Find each parasitized red blood cell.
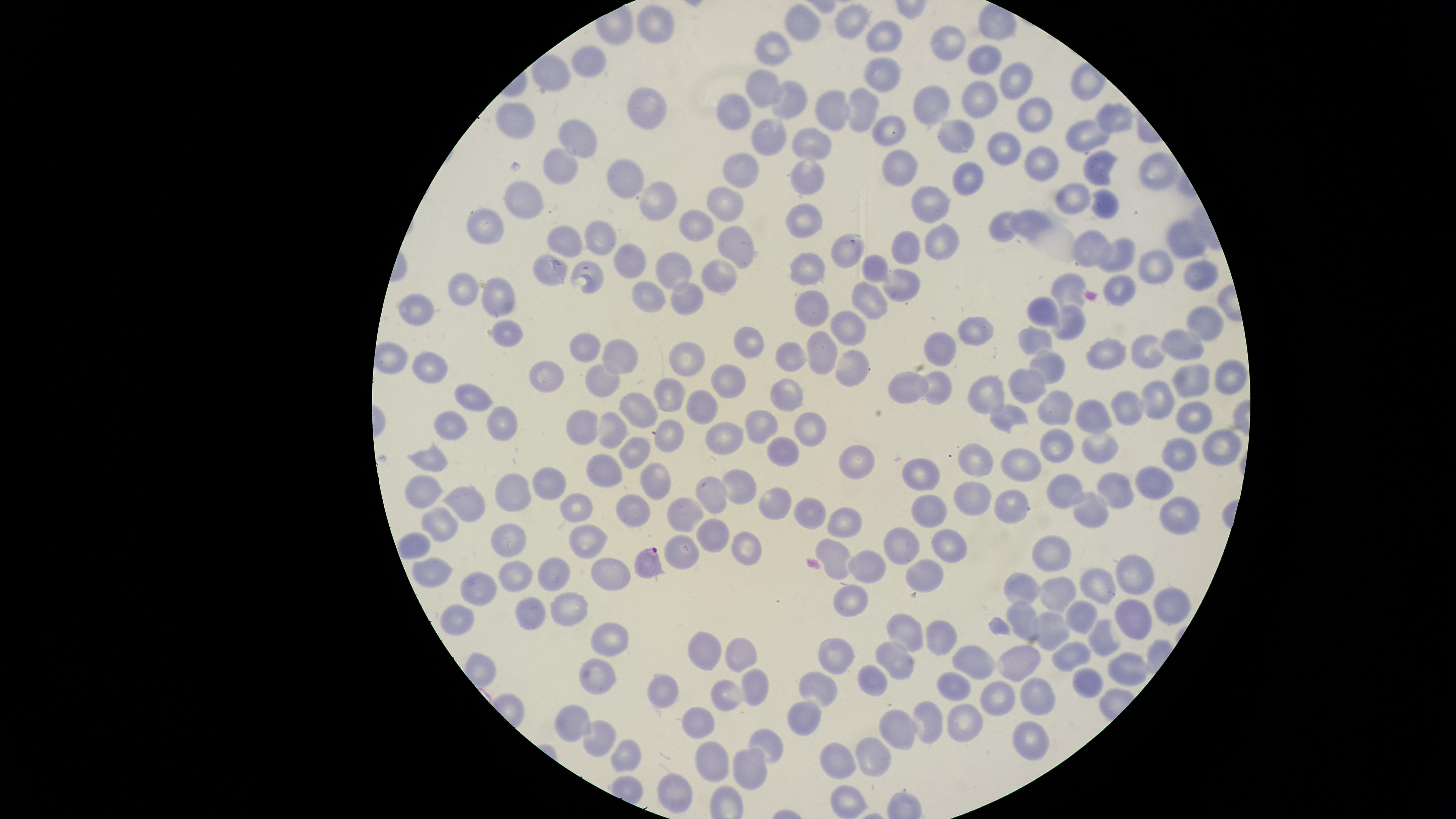
Approximate marker points, in pixels from the top-left corner.
Parasitized red blood cells: (x=644, y=564).

Approximate marker points, in pixels from the top-left corner. Uninfected red blood cells: (x=806, y=20), (x=853, y=20), (x=656, y=29), (x=889, y=32), (x=951, y=41), (x=779, y=48), (x=981, y=63), (x=592, y=64), (x=885, y=76), (x=1009, y=77), (x=765, y=81), (x=974, y=95), (x=796, y=101), (x=939, y=101), (x=742, y=109), (x=1034, y=109), (x=647, y=111), (x=838, y=112), (x=863, y=112), (x=1109, y=120), (x=517, y=121), (x=770, y=131), (x=957, y=134), (x=577, y=135), (x=892, y=135), (x=805, y=137), (x=1087, y=137), (x=1001, y=149), (x=571, y=158), (x=1040, y=164), (x=1150, y=168), (x=744, y=169), (x=1099, y=169), (x=898, y=172), (x=972, y=175), (x=805, y=179), (x=629, y=186), (x=1074, y=194), (x=928, y=200), (x=655, y=201), (x=1109, y=201), (x=522, y=202), (x=727, y=202), (x=1025, y=221), (x=805, y=223), (x=490, y=225), (x=693, y=225), (x=1003, y=232), (x=605, y=238), (x=942, y=238), (x=905, y=241), (x=560, y=242), (x=1181, y=242), (x=738, y=246), (x=1088, y=248), (x=847, y=250), (x=1121, y=252), (x=873, y=263), (x=632, y=264), (x=674, y=265), (x=1153, y=265), (x=551, y=268), (x=720, y=268), (x=809, y=268), (x=588, y=269), (x=1198, y=273), (x=903, y=278), (x=1123, y=286), (x=1065, y=287), (x=464, y=293), (x=651, y=293), (x=872, y=294), (x=689, y=295), (x=498, y=298), (x=813, y=302), (x=1045, y=305), (x=417, y=313), (x=1068, y=318), (x=852, y=320), (x=1204, y=327), (x=506, y=328), (x=974, y=335), (x=1038, y=337), (x=1184, y=342), (x=759, y=344), (x=942, y=346), (x=822, y=347), (x=583, y=348), (x=1144, y=352), (x=794, y=355), (x=619, y=356), (x=1109, y=361), (x=1050, y=362), (x=687, y=363), (x=848, y=363), (x=432, y=369), (x=1232, y=376), (x=549, y=377), (x=726, y=377), (x=602, y=379), (x=1191, y=381), (x=907, y=385), (x=1026, y=386), (x=940, y=388), (x=792, y=393), (x=661, y=394), (x=470, y=395), (x=986, y=395), (x=1155, y=395), (x=1061, y=404), (x=639, y=405), (x=703, y=405), (x=1122, y=408), (x=1097, y=414), (x=1198, y=415), (x=1006, y=416), (x=763, y=419), (x=499, y=425), (x=615, y=425), (x=448, y=427), (x=579, y=428), (x=813, y=431), (x=668, y=433), (x=725, y=434), (x=1060, y=441), (x=785, y=447), (x=631, y=448), (x=1102, y=449), (x=1229, y=449), (x=1174, y=454), (x=969, y=456), (x=858, y=458), (x=429, y=463), (x=1015, y=464), (x=605, y=467), (x=651, y=478), (x=924, y=479), (x=1153, y=480), (x=551, y=485), (x=735, y=485), (x=713, y=489), (x=1120, y=489), (x=1069, y=491), (x=518, y=493), (x=423, y=495), (x=971, y=497), (x=1005, y=502), (x=576, y=503), (x=632, y=506), (x=777, y=506), (x=463, y=508), (x=683, y=509), (x=812, y=511), (x=1174, y=512), (x=929, y=514), (x=1091, y=514), (x=843, y=518), (x=441, y=530), (x=712, y=535), (x=512, y=539), (x=418, y=543), (x=588, y=543), (x=899, y=543), (x=946, y=544), (x=684, y=547), (x=1059, y=547), (x=743, y=549), (x=836, y=552), (x=867, y=563), (x=550, y=568), (x=611, y=569), (x=435, y=572), (x=1132, y=572), (x=519, y=573), (x=924, y=573), (x=1026, y=583), (x=1108, y=583), (x=482, y=586), (x=1059, y=593), (x=856, y=598), (x=1171, y=601), (x=567, y=607), (x=528, y=611), (x=1023, y=613), (x=456, y=614), (x=1138, y=615), (x=1080, y=618), (x=904, y=625), (x=1055, y=629), (x=936, y=634), (x=1103, y=636), (x=605, y=642), (x=701, y=648), (x=743, y=651), (x=1075, y=655), (x=1017, y=656), (x=840, y=658), (x=901, y=658), (x=968, y=663), (x=1121, y=668), (x=873, y=680), (x=598, y=682), (x=757, y=683), (x=820, y=688), (x=951, y=689), (x=1084, y=689), (x=667, y=692), (x=724, y=698), (x=996, y=698), (x=1038, y=699), (x=807, y=713), (x=928, y=715), (x=700, y=723), (x=959, y=723), (x=574, y=724), (x=901, y=726), (x=1029, y=738), (x=763, y=744), (x=605, y=745), (x=876, y=753), (x=626, y=755), (x=845, y=756), (x=710, y=761), (x=750, y=767), (x=679, y=788), (x=845, y=793). Image is 1456×819 pixels. Thin blood smear. Giemsa stain. Single field of view. Smartphone photograph through the microscope eyepiece. Species: Plasmodium falciparum. The visible region is circular.